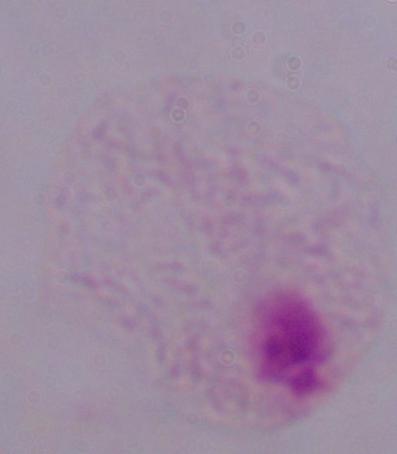 Captured at 1000x magnification. A trichomonad is shown. Micrograph.